State the preparation type.
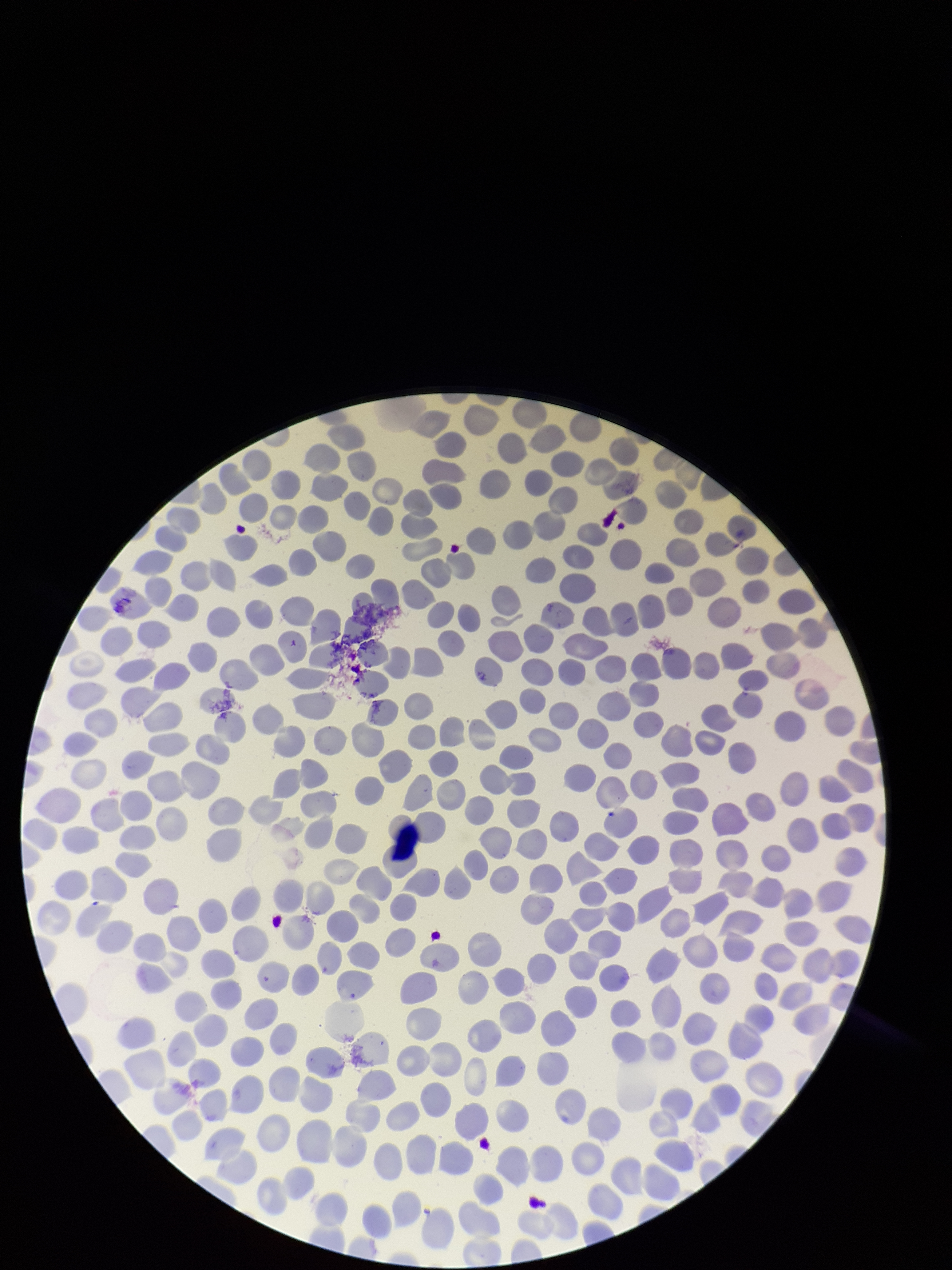
A thin smear.

stain: Giemsa
parasitized_red_blood_cells: none identified
patient_malaria_status: negative
red_blood_cell_count: 304
capture: smartphone photograph through the microscope eyepiece
parasitized_red_blood_cell_count: 0
field_of_view: one from this slide
image_size: 952×1270 pixels